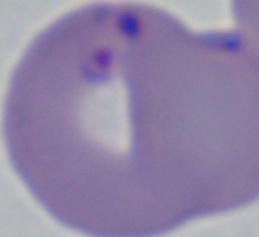
Summary:
  - Modality: photomicrograph
  - Identification: Babesia
  - Magnification: 1000x